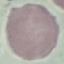

Summary:
  - Result: no malaria parasites detected
  - Image type: automatically extracted cell patch, resized to 64 × 64 pixels
  - Capture: smartphone through the microscope eyepiece
  - Stain: Giemsa
  - Preparation: thin blood film